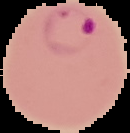
From a thin blood smear. Malaria status: parasitized. Segmented cell region on a black background. Image is 130×133 pixels.